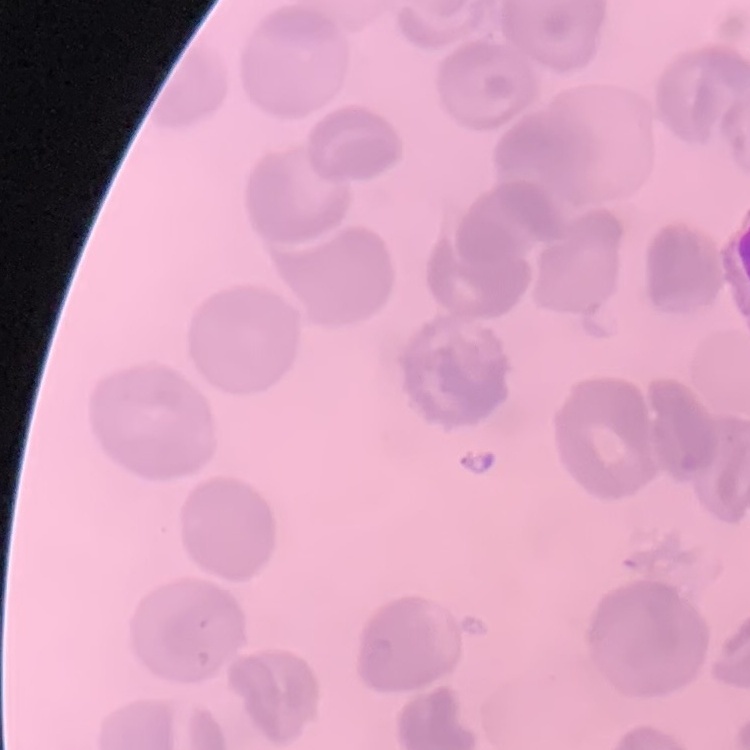
The red blood cells show no rouleaux formation. Thin blood film. Stained with either Field's or Giemsa. Square crop of a larger photomicrograph.